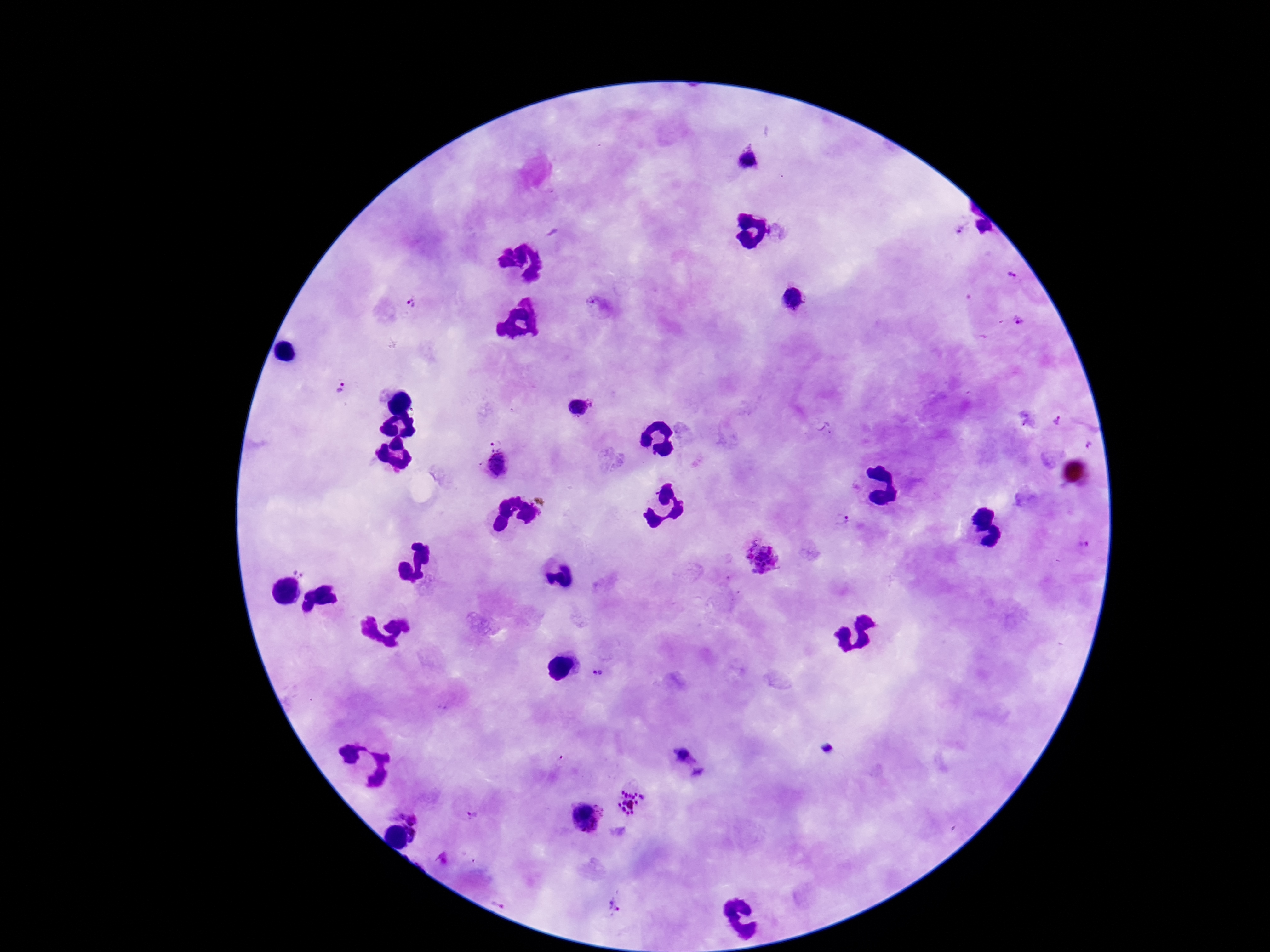 Approximate centers as (x, y) in pixels. Plasmodium parasite locations: (1011, 276), (793, 298), (412, 303), (601, 308), (1016, 320), (343, 388), (592, 400), (1057, 422), (495, 441), (1090, 445), (841, 520), (1082, 543), (759, 554), (598, 674), (685, 752), (630, 801), (407, 812), (469, 816), (415, 835), (616, 906). Giemsa-stained preparation. Thick peripheral-blood smear. 100x magnification. Single field of view. Image is 1270×952 pixels. Patient malaria status: infected. Photographed through the microscope eyepiece with a smartphone camera.